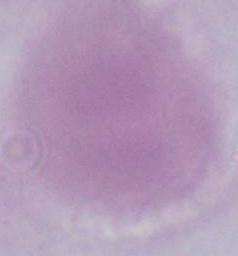

identification = red blood cell
magnification = 1000x
modality = micrograph